Locate every blood parasite and identify its species.
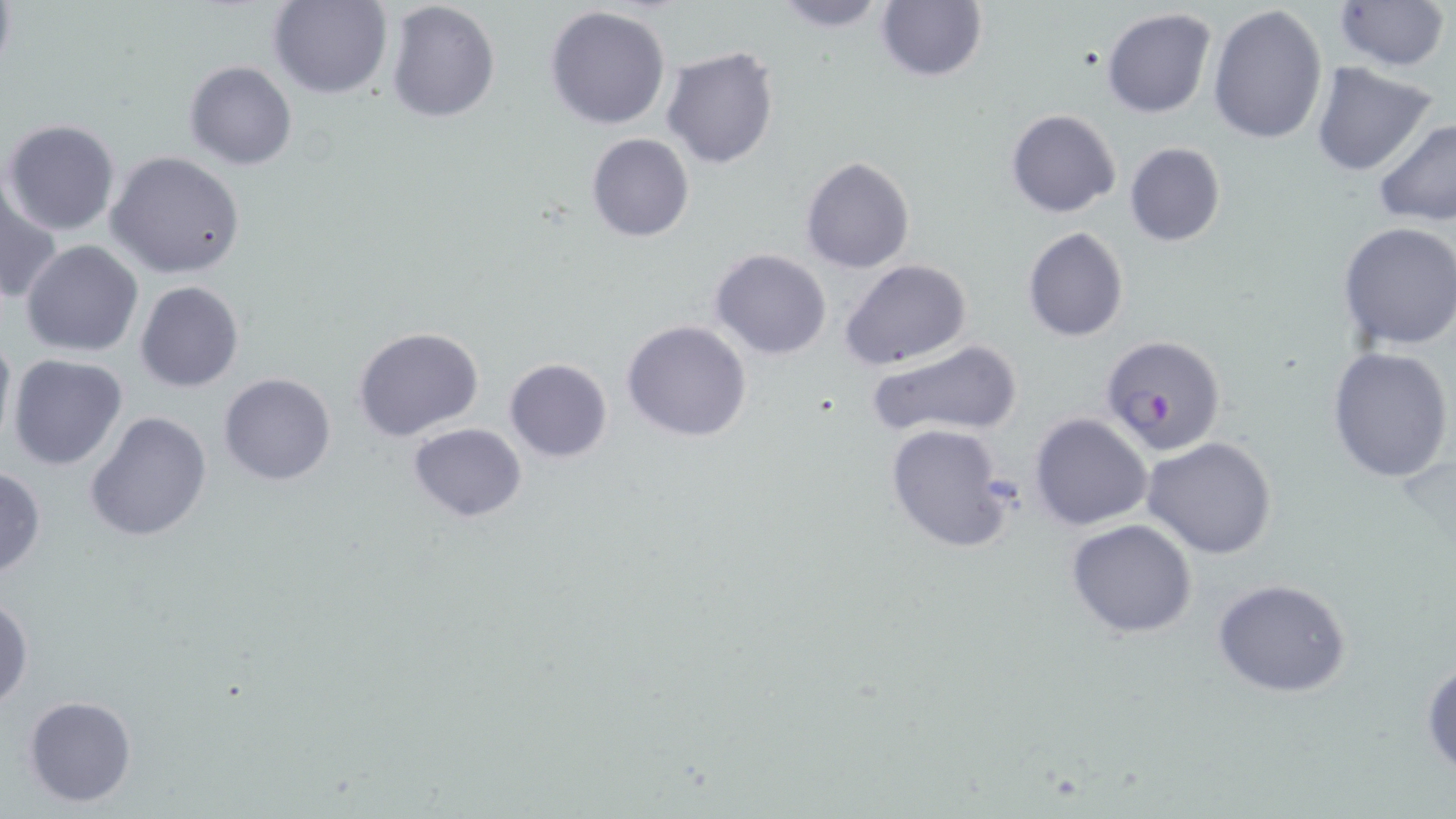

Approximate bounding boxes as [x1, y1, x2, y2] in pixels.
Plasmodium falciparum-infected red blood cells: [1100, 333, 1224, 458].
No Plasmodium ovale, Plasmodium malariae, Plasmodium vivax, Babesia divergens, or Trypanosoma brucei observed.

Uninfected red blood cell locations: [268, 0, 393, 99], [386, 0, 501, 122], [768, 0, 894, 32], [1333, 0, 1452, 75], [875, 1, 989, 82], [1206, 4, 1327, 143], [545, 6, 673, 130], [1102, 7, 1217, 118], [661, 45, 780, 170], [184, 61, 298, 170], [1310, 62, 1441, 178], [1005, 108, 1121, 217], [1372, 116, 1456, 228], [3, 118, 122, 236], [586, 133, 695, 242], [1124, 142, 1226, 246], [107, 150, 246, 279], [800, 156, 916, 274], [1, 174, 61, 308], [1337, 221, 1456, 353], [1021, 226, 1129, 343], [21, 239, 144, 356], [711, 249, 833, 361], [840, 259, 972, 371], [134, 280, 244, 392], [621, 319, 753, 442], [0, 323, 15, 454], [354, 326, 485, 443], [868, 338, 1025, 441], [1327, 346, 1454, 484], [7, 354, 128, 472], [503, 357, 614, 462], [219, 372, 337, 487], [84, 409, 214, 543], [1028, 413, 1154, 531], [407, 422, 528, 523], [884, 422, 1015, 554], [1142, 436, 1278, 558], [0, 465, 47, 580], [1066, 518, 1197, 638], [1211, 577, 1354, 698], [1, 594, 34, 710], [1422, 656, 1455, 777], [23, 696, 137, 806]. Slide-level diagnosis: Plasmodium falciparum. May-Grünwald-Giemsa stain. Captured at 1000x magnification. Thin blood smear. Image is 1456×819 pixels. Single field of view. Optical microscopy.